Outline each blood parasite and name the species.
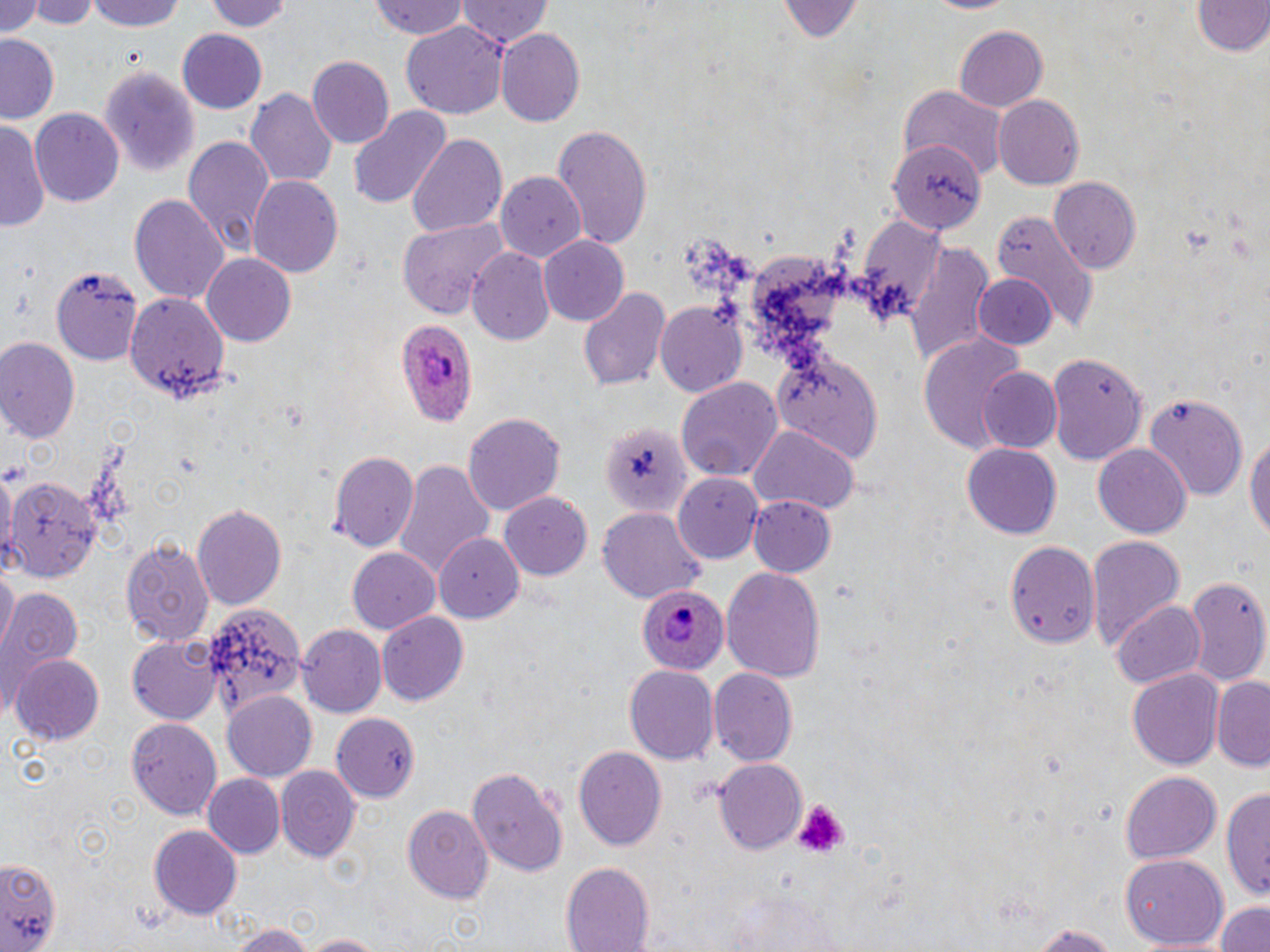
Approximate bounding boxes as named x1/y1/x2/y2 corners in pixels.
Plasmodium ovale-infected red blood cells: (x1=394, y1=321, x2=480, y2=426), (x1=637, y1=584, x2=732, y2=674).
No Plasmodium falciparum, Plasmodium malariae, Plasmodium vivax, Babesia divergens, or Trypanosoma brucei observed.

slide-level diagnosis = Plasmodium ovale
uninfected red blood cell locations = approximate bounding boxes as named x1/y1/x2/y2 corners in pixels: (x1=0, y1=0, x2=43, y2=39), (x1=27, y1=0, x2=96, y2=31), (x1=89, y1=0, x2=187, y2=32), (x1=370, y1=0, x2=472, y2=40), (x1=774, y1=0, x2=864, y2=44), (x1=919, y1=0, x2=1021, y2=16), (x1=1188, y1=0, x2=1269, y2=59), (x1=209, y1=1, x2=294, y2=33), (x1=456, y1=1, x2=551, y2=49), (x1=0, y1=4, x2=48, y2=75), (x1=403, y1=22, x2=507, y2=119), (x1=955, y1=24, x2=1049, y2=113), (x1=497, y1=28, x2=585, y2=125), (x1=175, y1=30, x2=268, y2=115), (x1=0, y1=35, x2=61, y2=123), (x1=309, y1=56, x2=396, y2=148), (x1=98, y1=66, x2=201, y2=176), (x1=901, y1=86, x2=1007, y2=182), (x1=247, y1=87, x2=337, y2=191), (x1=993, y1=94, x2=1085, y2=190), (x1=349, y1=105, x2=450, y2=209), (x1=29, y1=108, x2=124, y2=207), (x1=1, y1=122, x2=50, y2=233), (x1=552, y1=127, x2=654, y2=246), (x1=407, y1=133, x2=507, y2=239), (x1=182, y1=134, x2=276, y2=255), (x1=888, y1=140, x2=986, y2=234), (x1=496, y1=172, x2=588, y2=260), (x1=248, y1=173, x2=342, y2=277), (x1=1049, y1=177, x2=1142, y2=272), (x1=131, y1=193, x2=229, y2=305), (x1=992, y1=212, x2=1095, y2=334), (x1=396, y1=220, x2=505, y2=319), (x1=538, y1=236, x2=628, y2=325), (x1=905, y1=244, x2=995, y2=365), (x1=469, y1=248, x2=555, y2=346), (x1=201, y1=253, x2=296, y2=348), (x1=51, y1=266, x2=146, y2=365), (x1=973, y1=275, x2=1058, y2=351), (x1=578, y1=284, x2=670, y2=393), (x1=121, y1=293, x2=229, y2=403), (x1=655, y1=300, x2=748, y2=396), (x1=916, y1=332, x2=1030, y2=459), (x1=0, y1=338, x2=81, y2=446), (x1=770, y1=350, x2=884, y2=461), (x1=1045, y1=351, x2=1147, y2=464), (x1=978, y1=367, x2=1063, y2=454), (x1=677, y1=379, x2=781, y2=482), (x1=1144, y1=395, x2=1250, y2=499), (x1=464, y1=413, x2=565, y2=514), (x1=597, y1=420, x2=694, y2=517), (x1=748, y1=424, x2=856, y2=516), (x1=1244, y1=427, x2=1270, y2=551), (x1=961, y1=444, x2=1062, y2=538), (x1=1093, y1=446, x2=1191, y2=536), (x1=327, y1=448, x2=419, y2=553), (x1=389, y1=458, x2=495, y2=582), (x1=5, y1=474, x2=101, y2=582), (x1=677, y1=475, x2=761, y2=563), (x1=499, y1=490, x2=593, y2=580), (x1=747, y1=495, x2=838, y2=577), (x1=192, y1=503, x2=288, y2=608), (x1=598, y1=510, x2=705, y2=602), (x1=435, y1=531, x2=525, y2=621), (x1=1085, y1=535, x2=1185, y2=651), (x1=120, y1=536, x2=212, y2=647), (x1=1007, y1=540, x2=1102, y2=649), (x1=345, y1=546, x2=440, y2=634), (x1=1, y1=566, x2=17, y2=655), (x1=720, y1=566, x2=825, y2=682), (x1=1181, y1=574, x2=1267, y2=689), (x1=1, y1=587, x2=83, y2=700), (x1=1113, y1=602, x2=1208, y2=688), (x1=204, y1=605, x2=304, y2=717), (x1=376, y1=612, x2=467, y2=707), (x1=298, y1=625, x2=386, y2=720), (x1=127, y1=636, x2=222, y2=723), (x1=10, y1=653, x2=105, y2=744), (x1=624, y1=664, x2=719, y2=764), (x1=708, y1=669, x2=797, y2=767), (x1=1127, y1=670, x2=1225, y2=768), (x1=1212, y1=676, x2=1270, y2=771), (x1=223, y1=691, x2=319, y2=780), (x1=331, y1=712, x2=418, y2=801), (x1=127, y1=717, x2=223, y2=823), (x1=573, y1=746, x2=667, y2=850), (x1=713, y1=759, x2=808, y2=854), (x1=465, y1=762, x2=569, y2=877), (x1=276, y1=767, x2=361, y2=862), (x1=1120, y1=769, x2=1221, y2=863), (x1=202, y1=773, x2=285, y2=859), (x1=1219, y1=785, x2=1269, y2=902), (x1=403, y1=806, x2=494, y2=904), (x1=149, y1=825, x2=244, y2=919), (x1=1, y1=852, x2=60, y2=947), (x1=1118, y1=856, x2=1229, y2=951), (x1=559, y1=861, x2=656, y2=952), (x1=723, y1=892, x2=853, y2=952), (x1=1212, y1=899, x2=1270, y2=952), (x1=1026, y1=922, x2=1123, y2=951), (x1=230, y1=924, x2=312, y2=952), (x1=300, y1=932, x2=385, y2=952)
preparation = thin blood smear
image size = 1270×952 pixels
modality = light microscopy
stain = May-Grünwald-Giemsa
magnification = 1000x
field of view = single
platelet locations = approximate bounding boxes as named x1/y1/x2/y2 corners in pixels: (x1=795, y1=801, x2=846, y2=857)